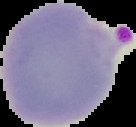

Summary:
  - Result: malaria parasites detected
  - Image size: 136×127 pixels
  - Image type: segmented cell region with the area outside set to black
  - Preparation: thin blood smear